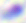

{
  "magnification": "400x",
  "identification": "Toxoplasma gondii",
  "modality": "micrograph"
}